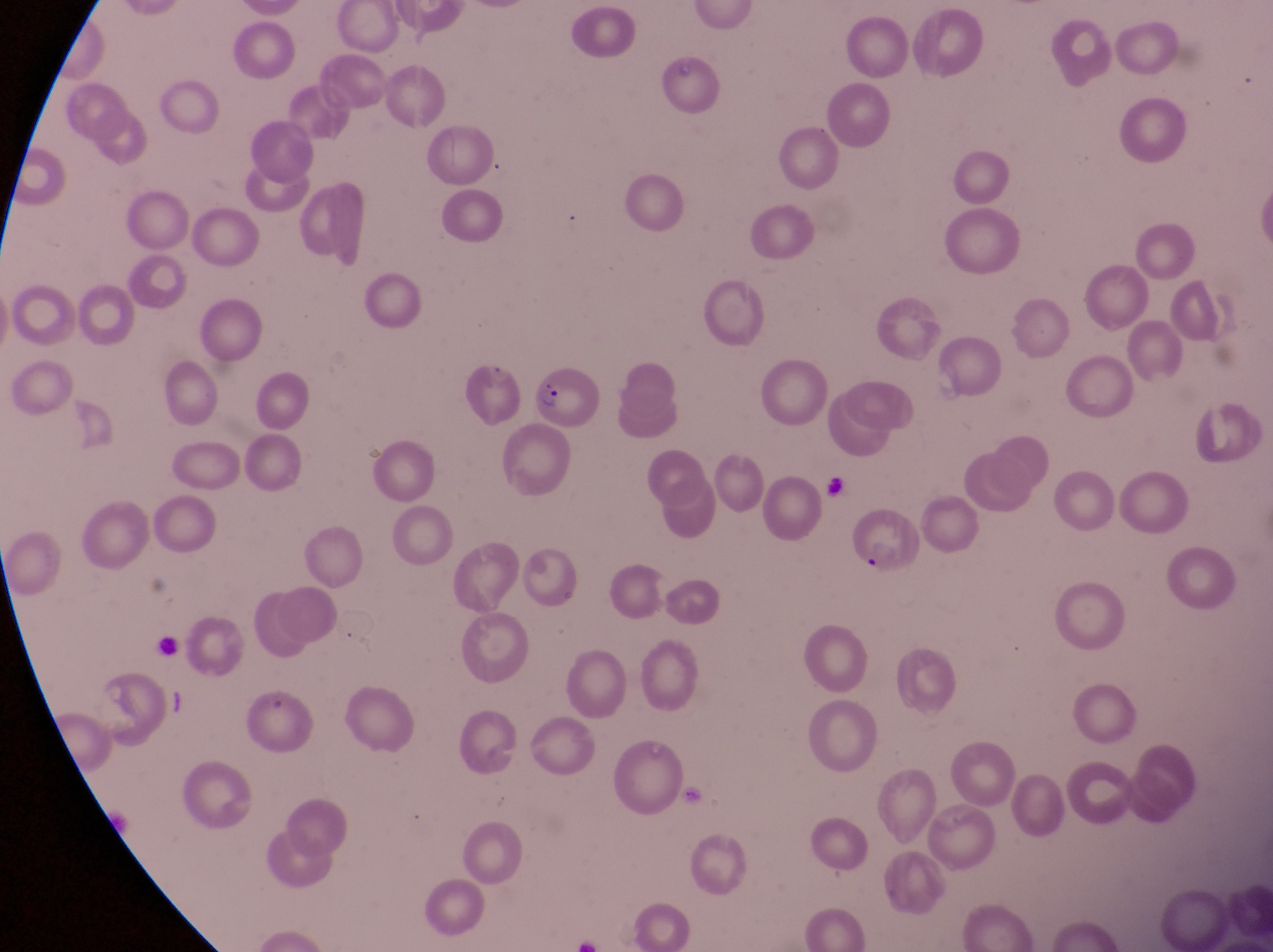
preparation = thin blood smear
magnification = 1000x
field of view = single
image size = 1273×952 pixels
capture = smartphone photograph through the eyepiece of an Olympus CX-23 microscope
parasitised red blood cell locations = approximate bounding boxes as left top right bottom in pixels: 530 367 602 427; 846 509 920 569
country = Uganda
artifact (platelet-like body, stain precipitate, or debris) locations = approximate bounding boxes as left top right bottom in pixels: 158 692 200 720